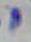

Summary:
  - Magnification: 1000x
  - Modality: photomicrograph
  - Identification: Toxoplasma gondii